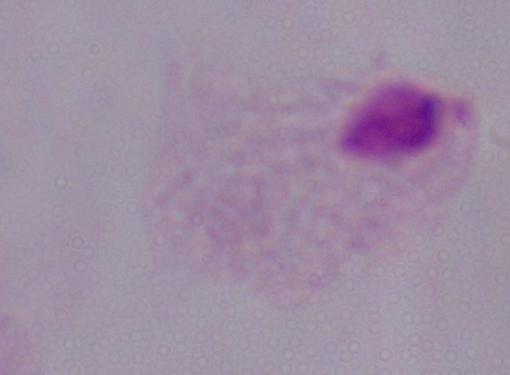 Photomicrograph. 1000x magnification. A trichomonad is seen.